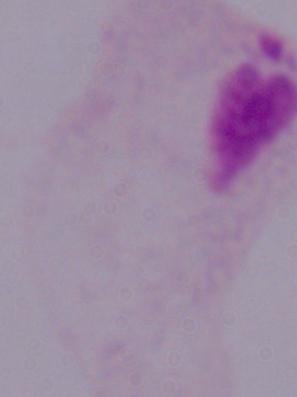
modality = photomicrograph
identification = trichomonad
magnification = 1000x